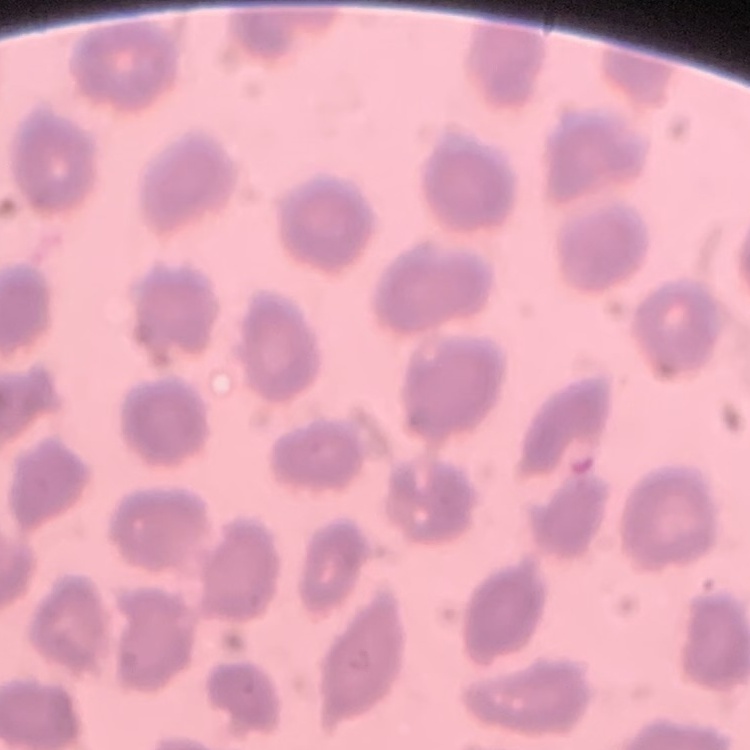 The red blood cells exhibit no rouleaux formation. Square crop of a larger photomicrograph. Stained with either Field's or Giemsa. Thin blood smear.